Evaluate for malaria.
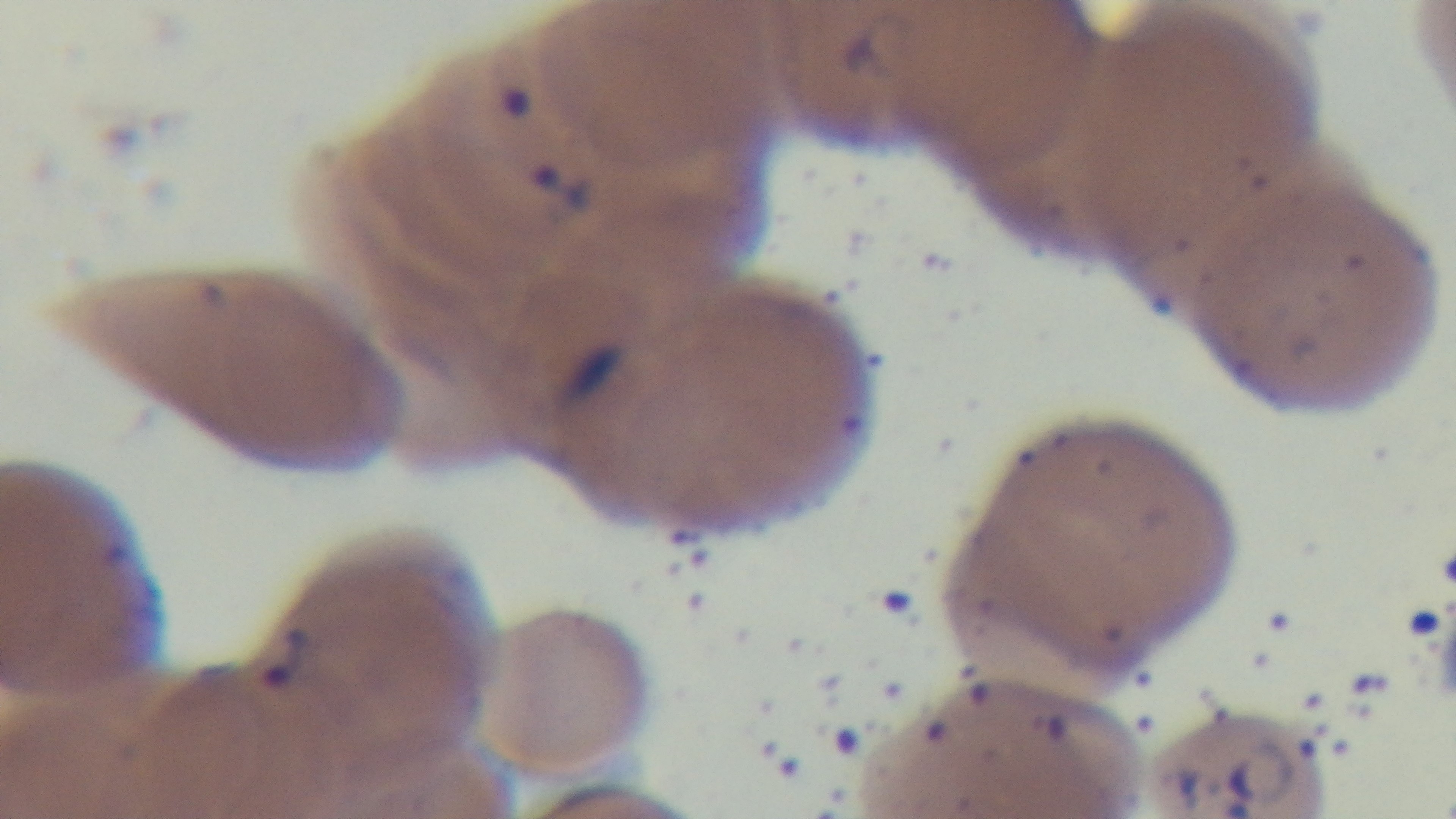

It is infected.

Summary:
  - Modality: light microscopy
  - Preparation: thin
  - Objective: 100x oil immersion
  - Field of view: single
  - Stain: Giemsa
  - Capture: mounted 4K digital camera